State the blood parasite species.
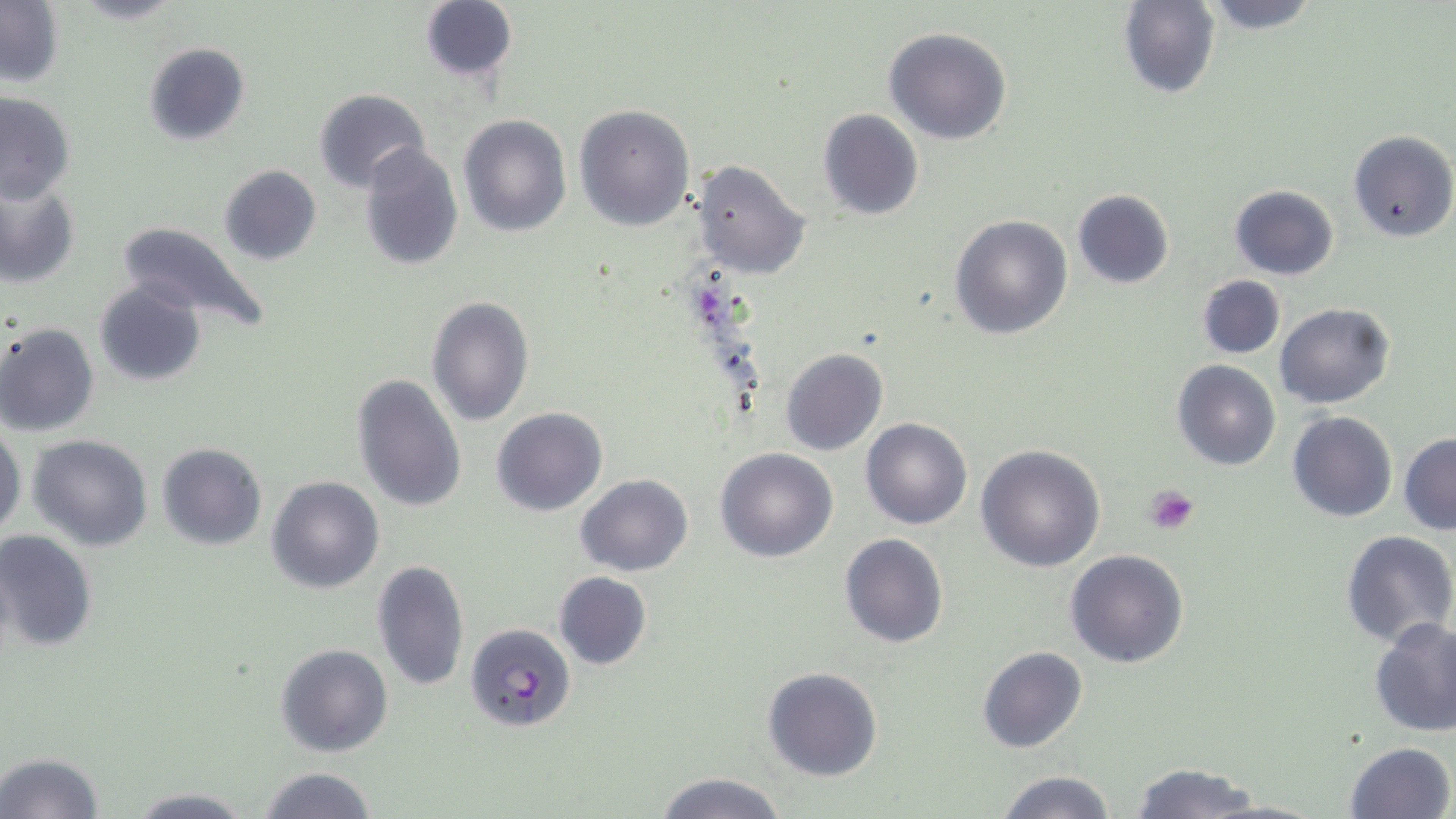

Plasmodium falciparum.

{
  "magnification": "1000x",
  "plasmodium_falciparum_infected_red_blood_cell_locations": "approximate bounding boxes as (x1, y1, x2, y2) in pixels: (465, 622, 576, 735)",
  "modality": "light microscopy",
  "field_of_view": "one of a larger specimen",
  "platelet_locations": "approximate bounding boxes as (x1, y1, x2, y2) in pixels: (1144, 484, 1199, 535)",
  "stain": "May-Grünwald-Giemsa",
  "image_size": "1456×819 pixels",
  "preparation": "thin blood smear",
  "uninfected_red_blood_cell_locations": "approximate bounding boxes as (x1, y1, x2, y2) in pixels: (0, 0, 63, 88), (69, 0, 188, 24), (1117, 0, 1220, 99), (1193, 0, 1324, 32), (419, 1, 519, 85), (884, 26, 1014, 145), (141, 42, 251, 147), (314, 89, 432, 194), (0, 90, 75, 205), (573, 102, 695, 232), (816, 109, 924, 221), (458, 115, 571, 238), (1348, 130, 1456, 242), (357, 142, 463, 270), (692, 160, 811, 280), (217, 164, 322, 266), (0, 180, 80, 289), (1229, 184, 1340, 280), (1071, 189, 1176, 290), (950, 215, 1072, 340), (115, 221, 272, 334), (1197, 275, 1285, 360), (94, 283, 207, 386), (427, 297, 534, 427), (1276, 302, 1394, 409), (0, 322, 100, 436), (779, 348, 888, 457), (1173, 360, 1280, 471), (352, 372, 468, 512), (492, 407, 607, 516), (1288, 412, 1398, 524), (861, 417, 973, 529), (0, 420, 25, 541), (1399, 433, 1456, 534), (27, 435, 153, 551), (156, 443, 268, 551), (977, 444, 1106, 572), (715, 448, 838, 563), (575, 473, 693, 576), (266, 475, 385, 593), (0, 530, 98, 652), (1341, 531, 1455, 646), (838, 532, 949, 649), (1064, 549, 1189, 669), (372, 560, 469, 691), (553, 572, 653, 671), (1370, 618, 1456, 737), (276, 644, 394, 757), (977, 647, 1088, 752), (761, 666, 885, 782), (1342, 741, 1453, 819), (0, 753, 105, 819), (1127, 762, 1265, 819), (255, 767, 378, 819), (996, 770, 1118, 819), (651, 773, 790, 819), (124, 789, 256, 818)"
}